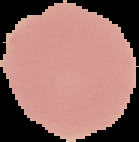

Summary:
  - Image type: segmented cell region on a black background
  - Preparation: thin blood film
  - Image size: 139×142 pixels
  - Result: no malaria parasites seen